Outline each blood parasite and name the species.
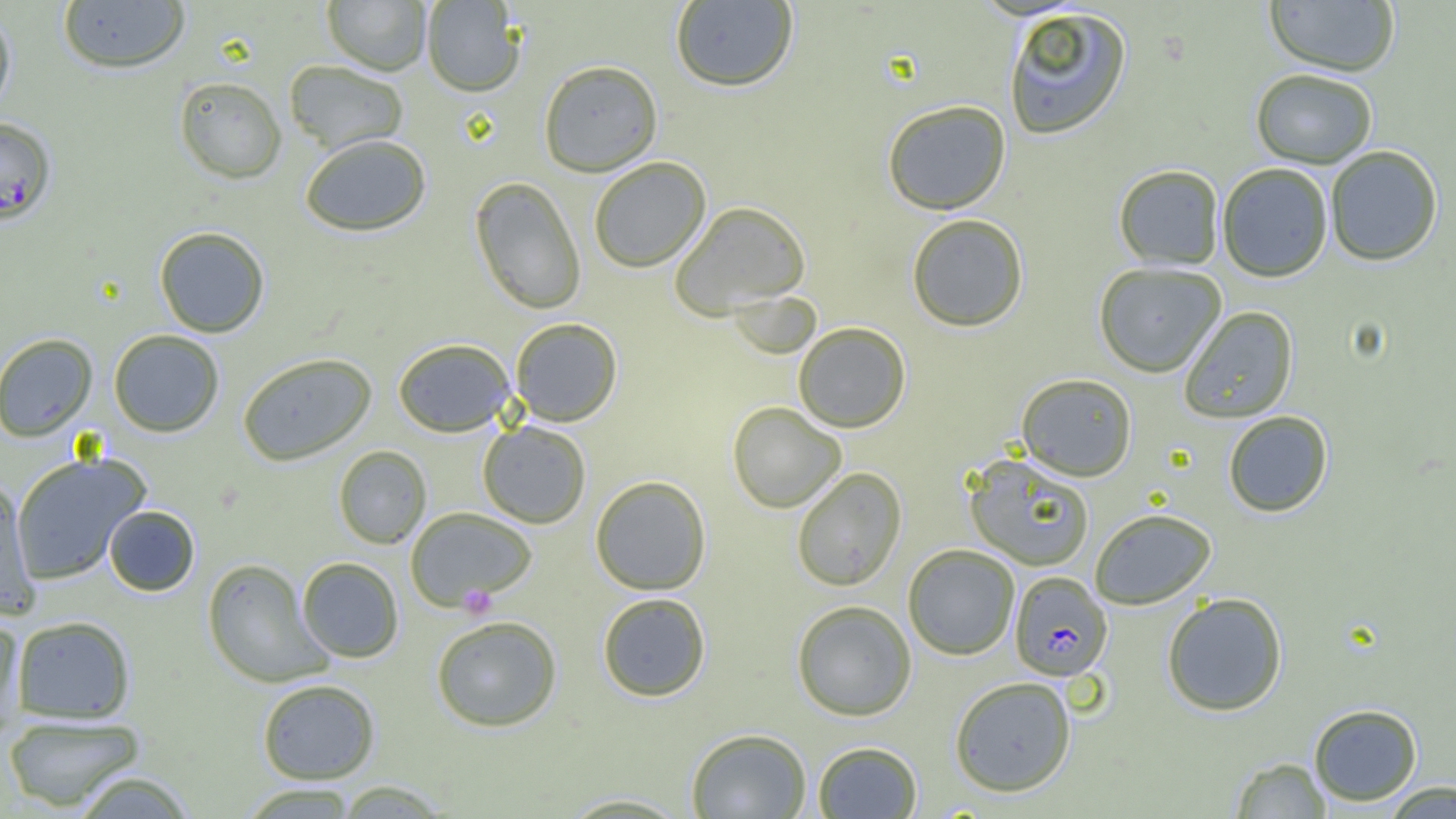
Approximate bounding boxes as named x1/y1/x2/y2 corners in pixels.
Plasmodium falciparum-infected red blood cells: (x1=0, y1=117, x2=57, y2=226), (x1=1009, y1=572, x2=1113, y2=680).
No Plasmodium ovale, Plasmodium malariae, Plasmodium vivax, Babesia divergens, or Trypanosoma brucei observed.

Platelet locations: (x1=458, y1=584, x2=498, y2=618). Uninfected red blood cell locations: (x1=58, y1=0, x2=190, y2=74), (x1=322, y1=0, x2=431, y2=75), (x1=421, y1=0, x2=525, y2=96), (x1=670, y1=0, x2=799, y2=92), (x1=1264, y1=0, x2=1400, y2=77), (x1=1003, y1=7, x2=1133, y2=141), (x1=0, y1=9, x2=17, y2=120), (x1=283, y1=60, x2=409, y2=155), (x1=538, y1=60, x2=663, y2=176), (x1=1250, y1=69, x2=1377, y2=168), (x1=174, y1=76, x2=287, y2=183), (x1=882, y1=100, x2=1011, y2=215), (x1=299, y1=133, x2=431, y2=237), (x1=1325, y1=145, x2=1443, y2=266), (x1=588, y1=156, x2=711, y2=273), (x1=1217, y1=163, x2=1334, y2=282), (x1=1113, y1=164, x2=1225, y2=270), (x1=469, y1=176, x2=587, y2=315), (x1=670, y1=201, x2=811, y2=319), (x1=906, y1=213, x2=1029, y2=332), (x1=154, y1=226, x2=270, y2=337), (x1=1093, y1=262, x2=1226, y2=377), (x1=1179, y1=306, x2=1299, y2=423), (x1=510, y1=317, x2=623, y2=426), (x1=793, y1=322, x2=911, y2=433), (x1=108, y1=329, x2=224, y2=437), (x1=0, y1=333, x2=98, y2=442), (x1=393, y1=338, x2=516, y2=437), (x1=237, y1=352, x2=377, y2=465), (x1=1016, y1=373, x2=1137, y2=481), (x1=727, y1=401, x2=847, y2=514), (x1=1222, y1=411, x2=1333, y2=517), (x1=477, y1=421, x2=592, y2=528), (x1=333, y1=445, x2=431, y2=549), (x1=10, y1=451, x2=150, y2=585), (x1=963, y1=454, x2=1095, y2=571), (x1=791, y1=467, x2=907, y2=591), (x1=590, y1=475, x2=712, y2=595), (x1=0, y1=480, x2=40, y2=618), (x1=103, y1=505, x2=200, y2=596), (x1=405, y1=507, x2=536, y2=609), (x1=1089, y1=508, x2=1217, y2=609), (x1=903, y1=544, x2=1020, y2=660), (x1=296, y1=557, x2=404, y2=663), (x1=201, y1=558, x2=330, y2=687), (x1=597, y1=592, x2=711, y2=701), (x1=1161, y1=592, x2=1288, y2=716), (x1=791, y1=600, x2=917, y2=721), (x1=12, y1=615, x2=136, y2=723), (x1=430, y1=615, x2=562, y2=731), (x1=0, y1=616, x2=27, y2=734), (x1=949, y1=676, x2=1077, y2=797), (x1=257, y1=678, x2=380, y2=784), (x1=1308, y1=703, x2=1423, y2=806), (x1=3, y1=714, x2=147, y2=813), (x1=686, y1=728, x2=812, y2=818), (x1=812, y1=741, x2=922, y2=818), (x1=1229, y1=757, x2=1332, y2=818), (x1=69, y1=770, x2=198, y2=818), (x1=331, y1=780, x2=454, y2=818), (x1=1380, y1=780, x2=1456, y2=818), (x1=238, y1=783, x2=361, y2=818), (x1=554, y1=792, x2=695, y2=817). Slide-level diagnosis: Plasmodium falciparum. Thin blood film. One field of a larger specimen. 1000x magnification. Optical microscopy. Image is 1456×819 pixels.